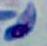

Summary:
  - Modality: photomicrograph
  - Identification: Toxoplasma gondii
  - Magnification: 1000x